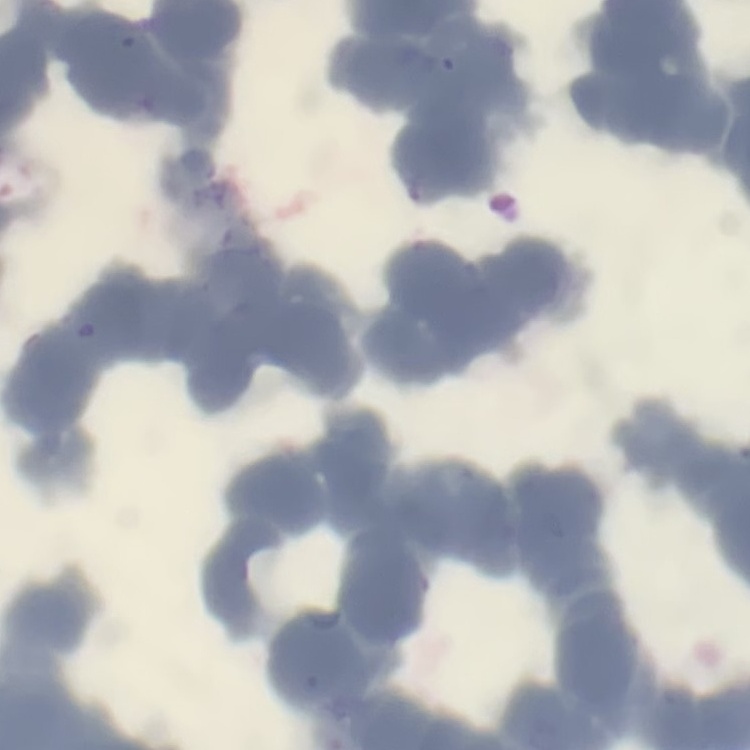
erythrocyte_morphology: rouleaux formation
stain: Field's or Giemsa
image_type: one tile cut from a larger photomicrograph
preparation: thin blood film